Outline each Plasmodium falciparum parasite and classify it by life-cycle stage.
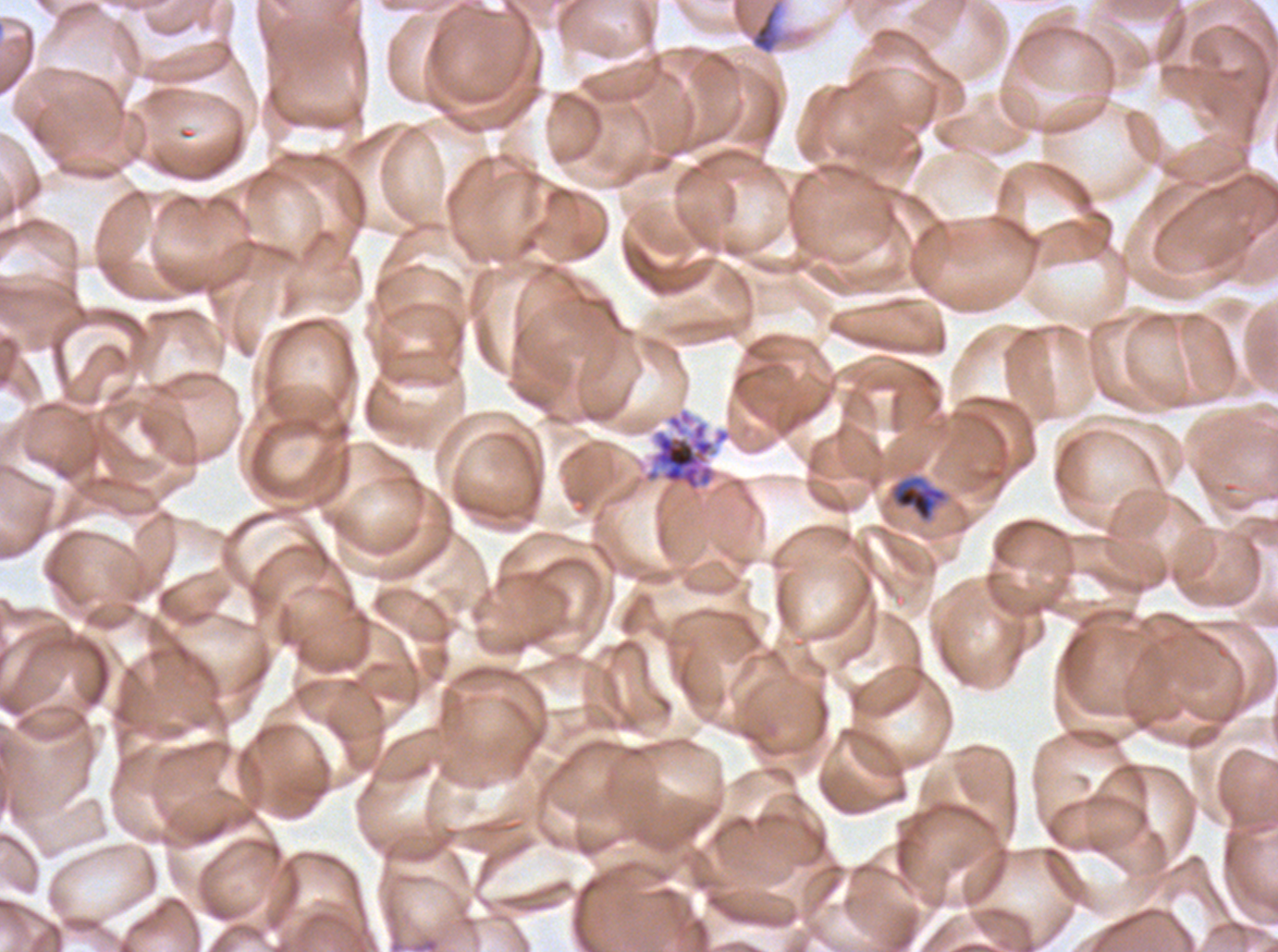
Approximate bounding rectangles given as corner coordinates in pixels from the top-left.
Mid trophozoites: (x1=890, y1=474, x2=949, y2=523).
Segmenters: (x1=642, y1=407, x2=732, y2=502).
No rings, late-ring/early-trophozoite forms, late trophozoites, early schizonts, late schizonts, or gametocytes observed.

Summary:
  - Debris locations: (x1=747, y1=0, x2=793, y2=55)
  - Preparation: thin blood smear
  - Life-cycle stages observed: mid trophozoite, segmenter
  - Field of view: sub-image separated from a larger composite
  - Specimen: Plasmodium falciparum cultured ex vivo for 24 to 48 hours, from a patient in The Gambia
  - Stain: Giemsa
  - Image size: 1278×952 pixels